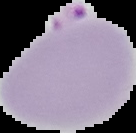

image type = segmented cell region with the area outside set to black
result = Plasmodium parasites detected
preparation = thin blood film
image size = 136×133 pixels